Comment on the morphology of the erythrocytes.
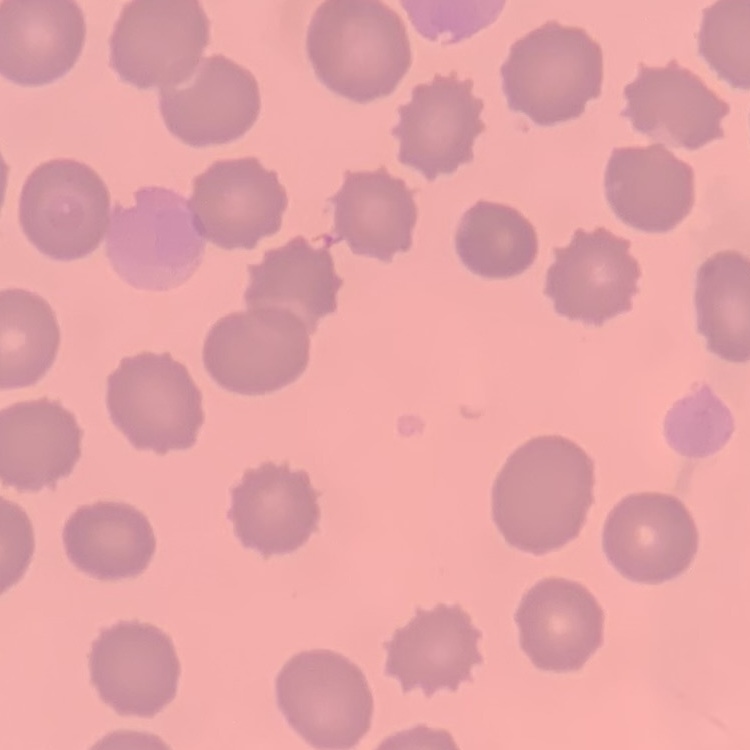

No rouleaux formation.

Summary:
  - Stain: Field's or Giemsa
  - Preparation: thin blood smear
  - Image type: one tile cut from a larger photomicrograph